Locate every malaria parasite.
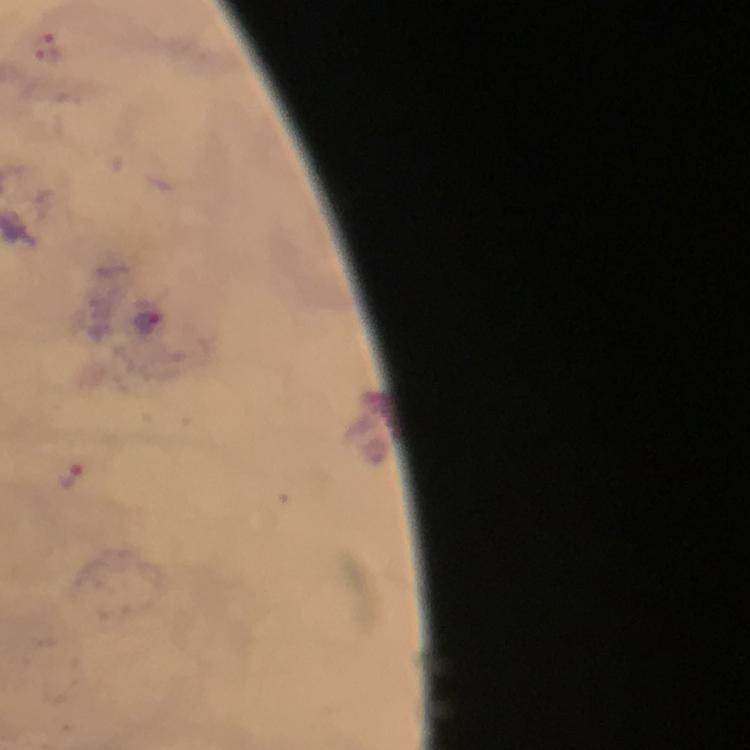

Approximate centers as [x, y] in pixels.
Malaria parasites: [146, 323], [72, 475].

Summary:
  - Context: from a diagnostic examination for malaria
  - Preparation: thick blood smear
  - Stain: Giemsa
  - Immersion oil: used
  - Magnification: 100x
  - Capture: smartphone photograph through a microscope
  - Cropped from: one field of view
  - Image size: 750×750 pixels